Classify this cell by malaria status.
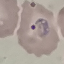

It is parasitized.

Summary:
  - Capture: smartphone through the microscope eyepiece
  - Stain: Giemsa
  - Preparation: thin blood smear
  - Image type: automatically extracted cell patch, resized to 64 × 64 pixels